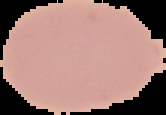

Summary:
  - Image type: segmented cell region with the area outside set to black
  - Preparation: thin blood film
  - Malaria status: uninfected
  - Image size: 166×115 pixels